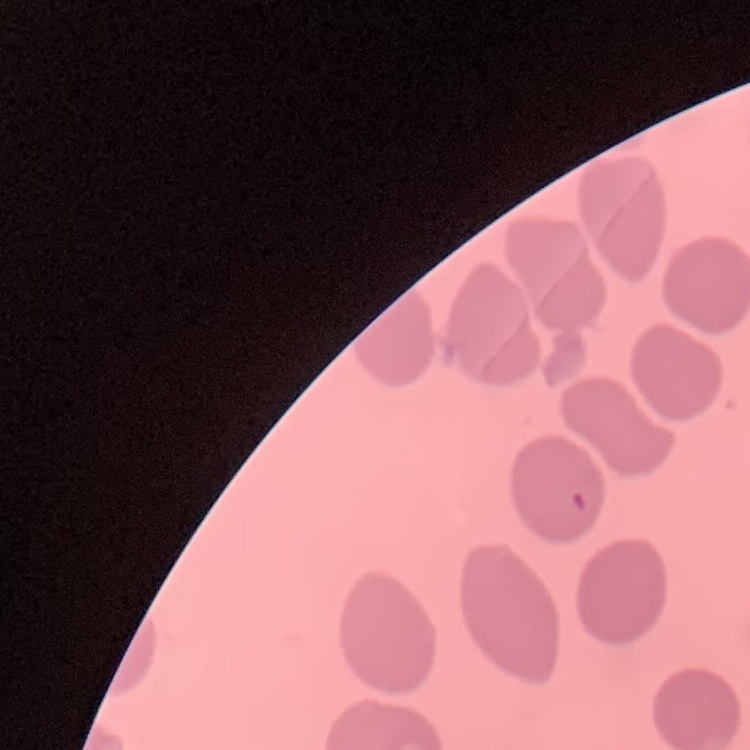

{
  "red_blood_cell_morphology": "no rouleaux formation",
  "stain": "Field's or Giemsa",
  "image_type": "one tile cut from a larger photomicrograph",
  "preparation": "thin blood smear"
}